Identify the parasite.
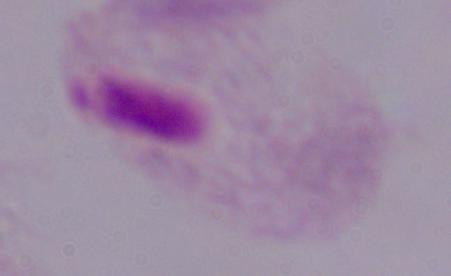

A trichomonad.

magnification = 1000x
modality = micrograph